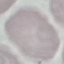

malaria status = uninfected
preparation = thin smear
capture = smartphone through the microscope eyepiece
stain = Giemsa
image type = automatically extracted cell patch, resized to 64 × 64 pixels